Locate and identify every blood parasite.
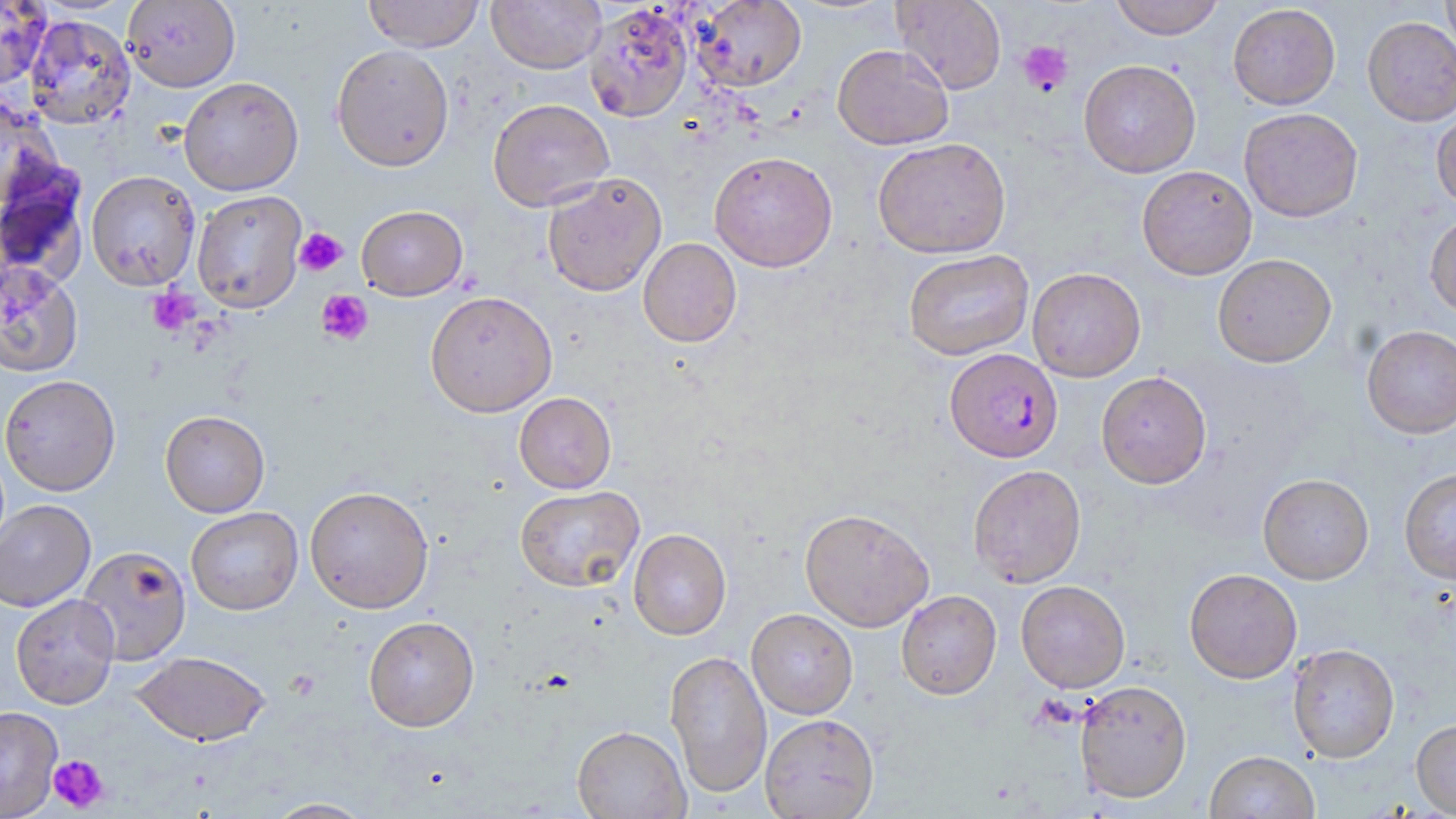
Approximate bounding boxes as (x1, y1, x2, y2) in pixels.
Plasmodium falciparum-infected red blood cells: (944, 348, 1063, 462).
No Plasmodium ovale, Plasmodium malariae, Plasmodium vivax, Babesia divergens, or Trypanosoma brucei observed.

Summary:
  - Platelet locations: (1018, 40, 1074, 96), (294, 228, 347, 277), (148, 288, 197, 336), (317, 290, 373, 346), (47, 754, 109, 812)
  - Uninfected red blood cell locations: (122, 0, 240, 92), (362, 0, 485, 52), (486, 0, 606, 74), (691, 0, 807, 92), (893, 0, 1006, 94), (1109, 0, 1224, 39), (1441, 0, 1456, 62), (0, 1, 50, 90), (584, 3, 693, 122), (1228, 4, 1340, 109), (23, 14, 136, 130), (1363, 17, 1456, 126), (331, 44, 455, 171), (832, 44, 954, 150), (1078, 59, 1201, 178), (178, 77, 304, 196), (0, 96, 62, 211), (488, 98, 614, 212), (1239, 108, 1363, 223), (1431, 109, 1456, 212), (872, 137, 1011, 258), (709, 151, 837, 272), (0, 162, 90, 288), (1137, 165, 1257, 280), (86, 171, 200, 292), (542, 172, 667, 297), (192, 191, 306, 313), (356, 205, 468, 300), (1425, 212, 1456, 319), (638, 238, 742, 347), (903, 249, 1034, 360), (1213, 253, 1336, 367), (0, 262, 84, 378), (1027, 267, 1146, 382), (425, 290, 557, 417), (1362, 325, 1456, 438), (1096, 371, 1212, 488), (1, 374, 121, 496), (514, 392, 616, 493), (160, 410, 270, 517), (968, 464, 1086, 587), (1399, 468, 1456, 584), (1257, 473, 1374, 584), (304, 485, 434, 614), (514, 485, 644, 592), (0, 499, 96, 612), (186, 507, 303, 615), (799, 508, 935, 632), (628, 528, 731, 640), (77, 545, 191, 665), (1184, 568, 1302, 683), (1015, 580, 1130, 693), (896, 590, 1001, 700), (10, 594, 120, 710), (746, 608, 858, 719), (363, 616, 480, 732), (1287, 643, 1400, 763), (665, 649, 772, 798), (133, 651, 270, 746), (1074, 679, 1192, 803), (0, 706, 63, 818), (760, 713, 879, 819), (1411, 718, 1456, 816), (571, 725, 690, 818), (1205, 750, 1319, 819), (263, 798, 375, 818)
  - Slide-level diagnosis: Plasmodium falciparum
  - Modality: optical microscopy
  - Stain: May-Grünwald-Giemsa
  - Image size: 1456×819 pixels
  - Preparation: thin blood smear
  - Magnification: 1000x
  - Field of view: one of a larger specimen